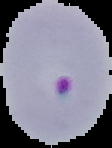
Malaria status: parasitized. Image is 112×148 pixels. From a thin blood film. Segmented cell region on a black background.